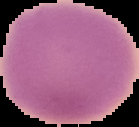
image size = 139×127 pixels
preparation = thin blood film
image type = cell region segmented out of the field of view; surrounding area masked to black
malaria status = uninfected